Identify the cell.
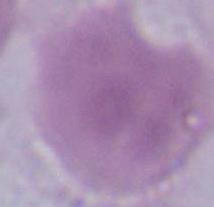
This is an erythrocyte.

Summary:
  - Modality: micrograph
  - Magnification: 1000x